Assess the morphology of the red blood cells.
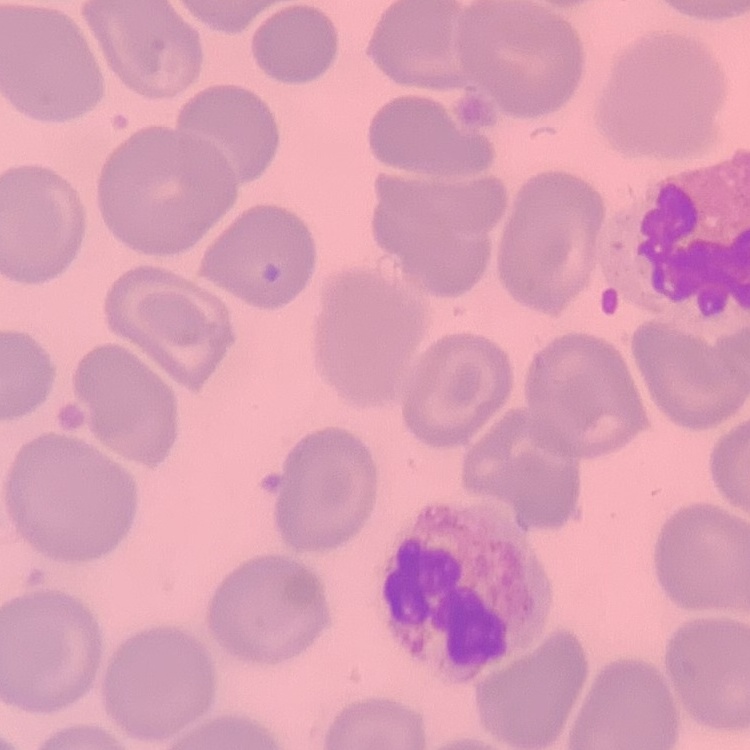

They show no rouleaux formation.

Stained with either Field's or Giemsa. Square crop of a larger photomicrograph. Thin blood smear.